Report the malaria status of this cell.
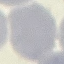
It is uninfected.

preparation: thin blood smear
image_type: cell patch, automatically extracted from a larger field of view and resized to 64 × 64 pixels
capture: smartphone camera at the microscope eyepiece
stain: Giemsa